Assess this cell for malaria.
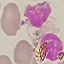
It is uninfected.

Summary:
  - Preparation: thin blood film
  - Capture: smartphone through the microscope eyepiece
  - Stain: Giemsa
  - Image type: automatically extracted cell patch, resized to 64 × 64 pixels